State which parasite is depicted.
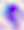
Toxoplasma gondii.

400x magnification. Micrograph.